Point out every Plasmodium parasite and every leukocyte.
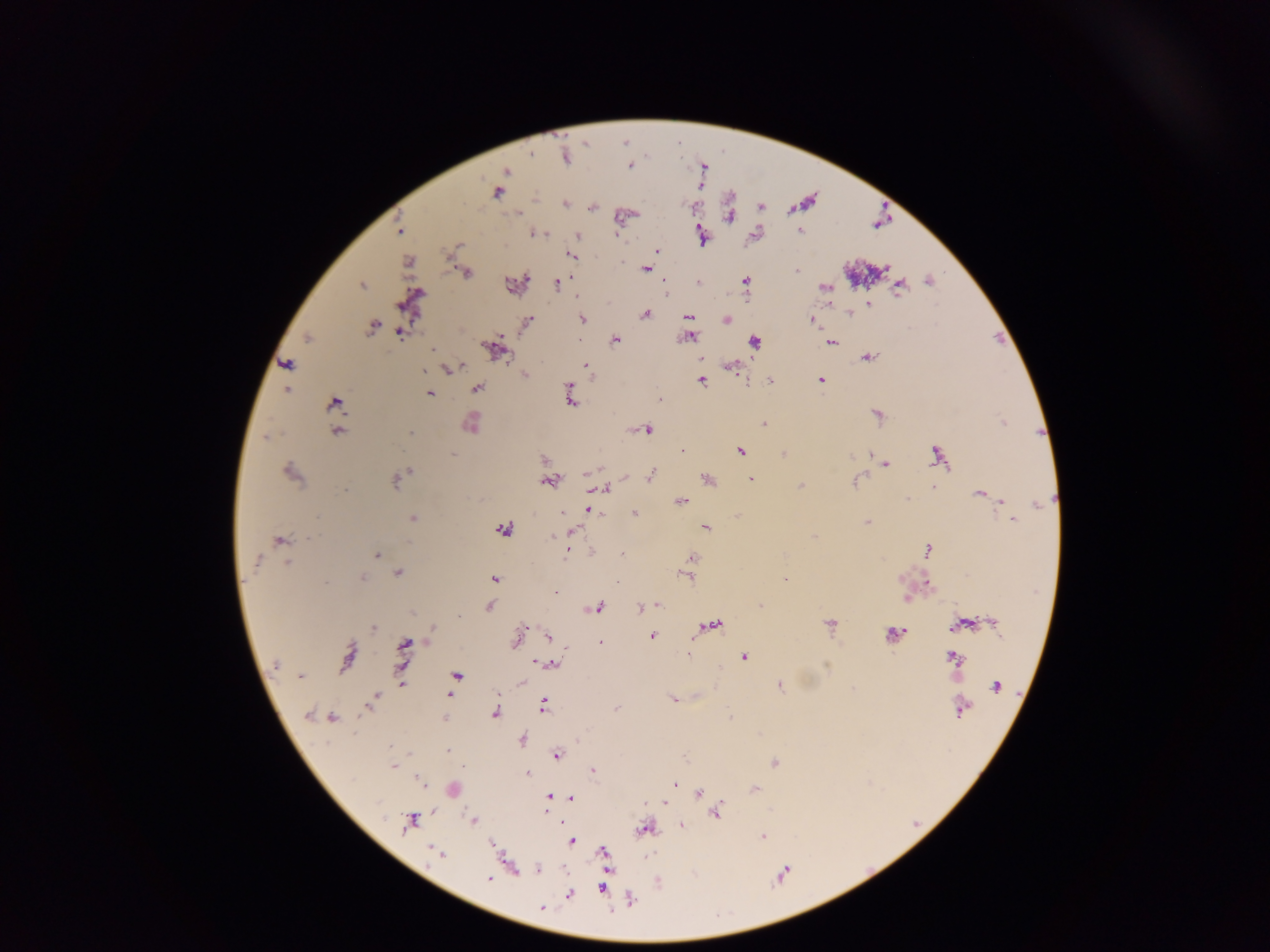
Approximate centers as [x, y] in pixels.
Plasmodium parasites: [566, 155], [631, 165], [505, 171], [497, 190], [565, 203], [591, 207], [759, 207], [729, 217], [799, 229], [399, 231], [534, 232], [755, 234], [576, 236], [701, 236], [456, 244], [658, 250], [570, 255], [408, 262], [645, 268], [464, 272], [797, 272], [929, 280], [663, 282], [697, 282], [745, 282], [516, 283], [556, 283], [361, 284], [898, 286], [824, 287], [411, 302], [869, 305], [849, 312], [644, 315], [688, 317], [582, 319], [726, 320], [527, 321], [814, 321], [373, 326], [405, 328], [400, 331], [689, 336], [308, 337], [615, 339], [578, 340], [753, 341], [830, 342], [494, 349], [432, 350], [867, 356], [286, 364], [585, 366], [731, 366], [449, 367], [525, 374], [701, 379], [820, 380], [746, 381], [770, 381], [286, 388], [476, 389], [429, 393], [568, 394], [660, 400], [334, 402], [877, 415], [1003, 422], [470, 423], [763, 423], [647, 429], [337, 431], [268, 436], [740, 450], [683, 451], [784, 453], [453, 455], [851, 455], [868, 455], [936, 457], [543, 459], [886, 464], [290, 472], [587, 472], [650, 476], [625, 478], [751, 478], [395, 479], [707, 479], [549, 481], [853, 482], [801, 486], [932, 486], [601, 489], [980, 493], [907, 499], [1001, 501], [680, 502], [1039, 505], [589, 509], [561, 512], [633, 513], [412, 518], [1012, 519], [866, 522], [705, 526], [502, 529], [571, 530], [552, 535], [813, 536], [279, 541], [927, 550], [566, 551], [376, 555], [691, 558], [687, 569], [398, 572], [684, 575], [361, 576], [493, 579], [617, 581], [784, 581], [926, 583], [554, 591], [906, 599], [657, 605], [759, 605], [488, 606], [598, 607], [642, 608], [993, 623], [962, 624], [710, 625], [829, 625], [374, 627], [524, 629], [892, 634], [652, 635], [548, 636], [517, 637], [600, 643], [404, 646], [688, 654], [744, 656], [348, 657], [952, 657], [539, 663], [552, 663], [275, 665], [301, 676], [456, 676], [520, 682], [401, 684], [780, 686], [996, 686], [448, 694], [673, 699], [372, 700], [542, 704], [615, 708], [961, 708], [495, 712], [308, 715], [332, 717], [444, 717], [730, 718], [521, 739], [448, 750], [556, 754], [774, 762], [393, 766], [591, 771], [527, 773], [674, 784], [453, 788], [754, 789], [697, 794], [549, 797], [571, 797], [664, 803], [715, 811], [546, 812], [409, 821], [473, 821], [680, 824], [645, 827], [763, 835], [571, 841], [492, 844], [603, 851], [437, 854], [508, 864], [537, 869], [489, 877], [602, 887], [568, 894], [631, 899], [541, 909].
No leukocytes observed.

Summary:
  - Capture: mobile-phone photograph through a microscope
  - Preparation: thick blood film
  - Image size: 1270×952 pixels
  - Field of view: single
  - Country: Ghana